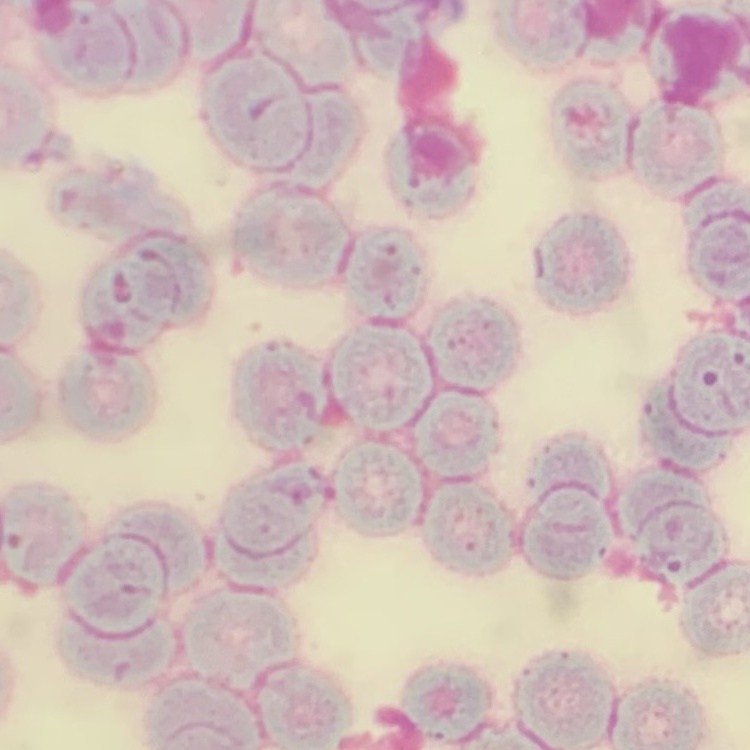 The erythrocytes show rouleaux formation. Thin peripheral smear. Square crop of a larger photomicrograph. Stained with either Field's or Giemsa.